Classify this cell by malaria status.
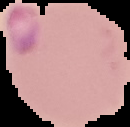

Parasitized.

From a thin blood film. The area outside the segmented cell region is set to black. Image is 130×127 pixels.